Report the malaria status of this cell.
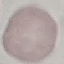
Uninfected.

image type = cell patch, automatically extracted from a larger field of view and resized to 64 × 64 pixels
preparation = thin blood smear
capture = smartphone camera at the microscope eyepiece
stain = Giemsa